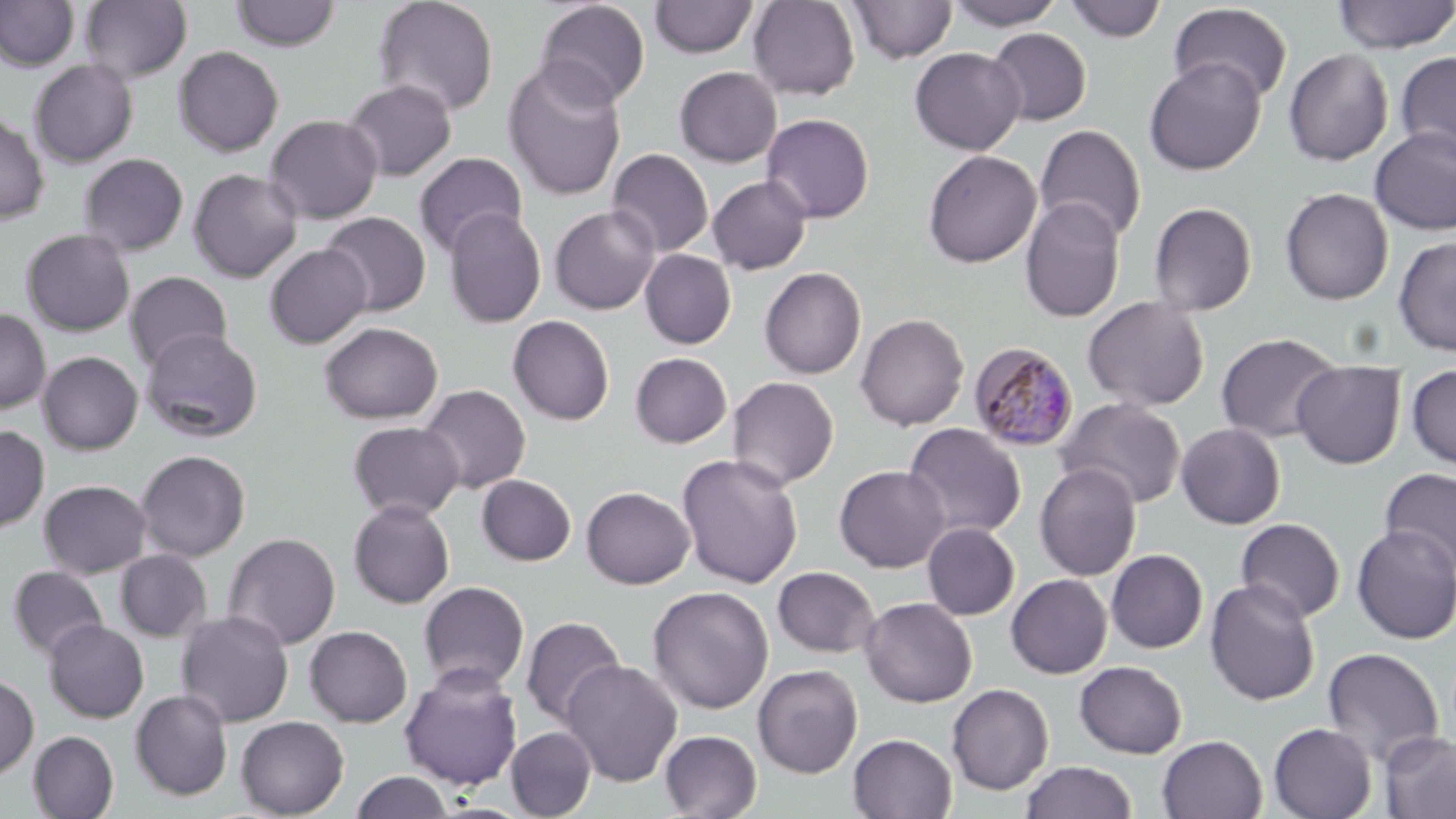
slide-level diagnosis = Plasmodium malariae
modality = light microscopy
image size = 1456×819 pixels
magnification = 1000x
uninfected red blood cell locations = approximate bounding boxes as [x1, y1, x2, y2] in pixels: [0, 0, 79, 71], [373, 0, 499, 117], [649, 0, 758, 58], [747, 0, 860, 100], [948, 0, 1063, 30], [1332, 0, 1456, 54], [79, 1, 192, 83], [230, 1, 341, 51], [535, 1, 651, 108], [848, 1, 958, 64], [1062, 1, 1167, 42], [1168, 3, 1294, 104], [987, 28, 1091, 126], [173, 46, 284, 157], [909, 47, 1026, 155], [1283, 48, 1394, 166], [1396, 51, 1456, 164], [1144, 57, 1267, 176], [502, 58, 628, 202], [29, 60, 138, 168], [674, 66, 782, 167], [341, 79, 457, 181], [0, 113, 49, 224], [762, 113, 874, 223], [264, 114, 383, 224], [1034, 124, 1147, 243], [1370, 126, 1456, 236], [607, 148, 714, 257], [922, 150, 1041, 268], [413, 152, 528, 257], [78, 153, 188, 256], [78, 163, 304, 266], [188, 168, 302, 282], [707, 175, 812, 274], [1279, 187, 1394, 305], [1020, 196, 1125, 323], [1149, 202, 1257, 316], [548, 205, 660, 314], [443, 209, 547, 328], [319, 212, 431, 316], [21, 229, 135, 336], [1393, 236, 1456, 357], [265, 244, 372, 348], [640, 249, 737, 349], [759, 267, 867, 379], [125, 271, 233, 372], [1082, 296, 1210, 411], [0, 309, 51, 414], [855, 313, 970, 430], [508, 315, 615, 424], [319, 321, 443, 424], [140, 328, 263, 442], [1216, 332, 1343, 443], [38, 351, 143, 455], [630, 352, 733, 448], [1291, 361, 1406, 469], [1406, 365, 1456, 470], [727, 376, 839, 490], [418, 384, 531, 494], [1056, 397, 1187, 509], [347, 421, 465, 520], [903, 422, 1027, 540], [1176, 423, 1286, 529], [0, 425, 49, 534], [136, 450, 250, 561], [677, 453, 804, 588], [1034, 462, 1142, 581], [834, 464, 949, 572], [1379, 467, 1456, 577], [477, 474, 576, 566], [39, 479, 152, 578], [581, 486, 695, 589], [348, 499, 455, 608], [1235, 518, 1345, 622], [922, 522, 1020, 621], [1235, 522, 1454, 633], [1351, 524, 1456, 645], [223, 532, 340, 650], [115, 549, 211, 642], [1106, 549, 1208, 653], [7, 566, 108, 660], [772, 566, 880, 658], [1006, 574, 1112, 678], [1205, 579, 1321, 706], [418, 581, 530, 692], [647, 586, 773, 714], [860, 597, 977, 707], [175, 609, 294, 727], [520, 616, 626, 728], [44, 620, 149, 723], [305, 625, 412, 728], [1322, 646, 1444, 768], [560, 659, 683, 786], [1074, 661, 1187, 758], [752, 664, 863, 778], [398, 665, 523, 790], [0, 673, 38, 780], [946, 683, 1053, 795], [130, 690, 234, 801], [235, 716, 349, 819], [1268, 722, 1377, 819], [506, 727, 596, 818], [659, 730, 762, 818], [1379, 730, 1456, 819], [28, 731, 119, 819], [848, 733, 957, 818], [1157, 735, 1267, 819], [1019, 761, 1138, 819], [350, 771, 456, 818]
preparation = thin blood smear
stain = May-Grünwald-Giemsa
Plasmodium malariae-infected red blood cell locations = approximate bounding boxes as [x1, y1, x2, y2] in pixels: [969, 342, 1079, 452]
field of view = one of a larger specimen